State which parasite is depicted.
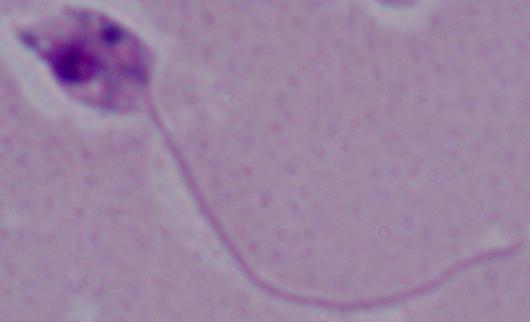

Leishmania.

Summary:
  - Modality: micrograph
  - Magnification: 1000x